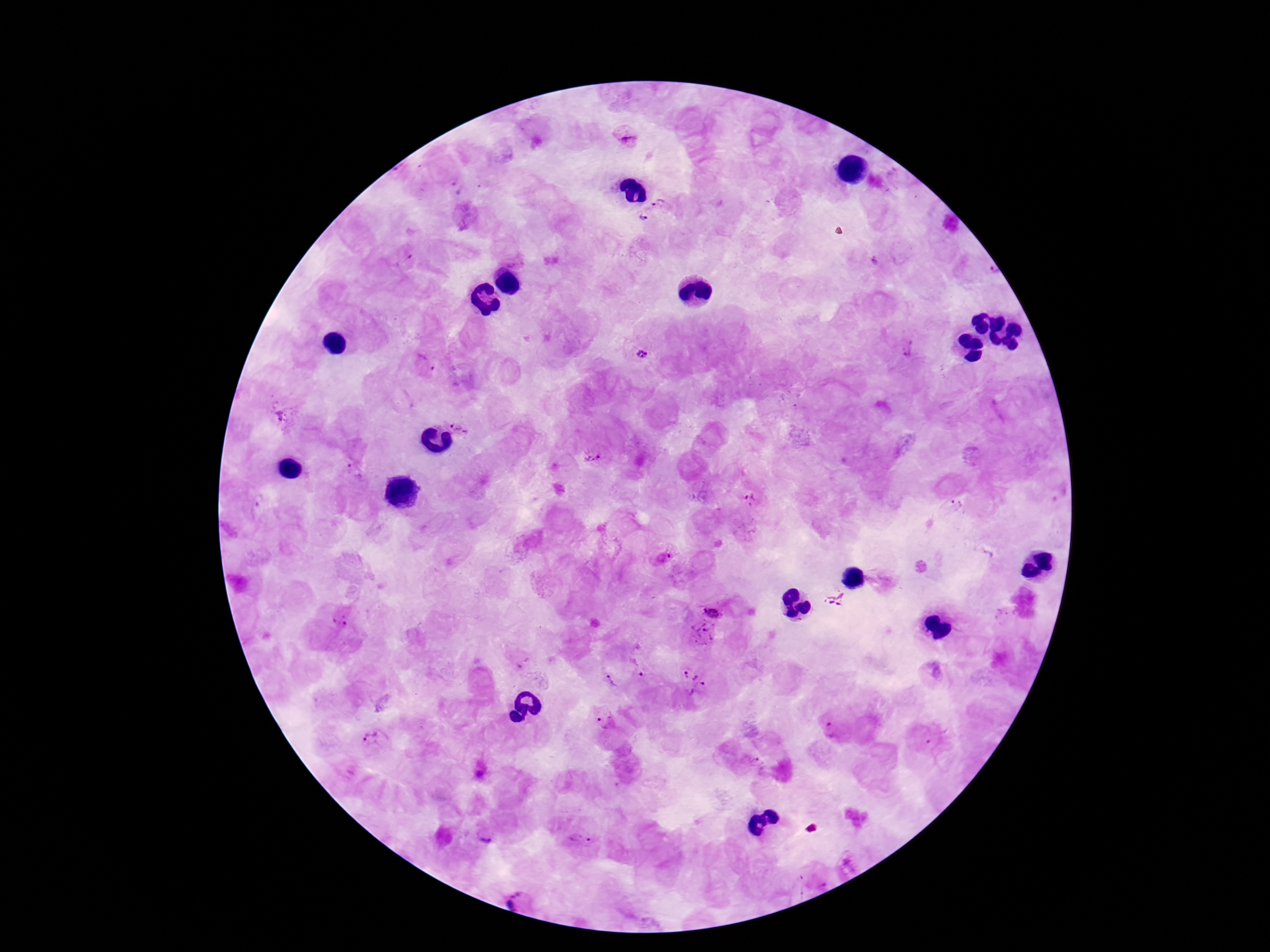

Approximate centers as (x, y) in pixels. Plasmodium parasite locations: (626, 137), (661, 201), (641, 218), (992, 271), (907, 347), (641, 354), (424, 365), (286, 416), (461, 425), (592, 458), (355, 470), (751, 500), (957, 504), (836, 597), (718, 604), (342, 619), (705, 632), (639, 667), (611, 681), (692, 683), (604, 721), (829, 731), (373, 739), (927, 739), (759, 762), (485, 838), (581, 838), (518, 901). Giemsa-stained preparation. 100x magnification. Photographed through the microscope eyepiece with a smartphone camera. Thick peripheral-blood smear. One field from this slide. Patient malaria status: infected. Image is 1270×952 pixels.